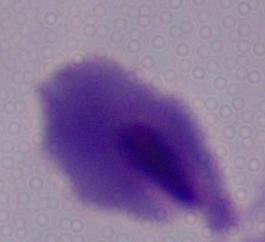

Summary:
  - Identification: trichomonad
  - Modality: micrograph
  - Magnification: 1000x